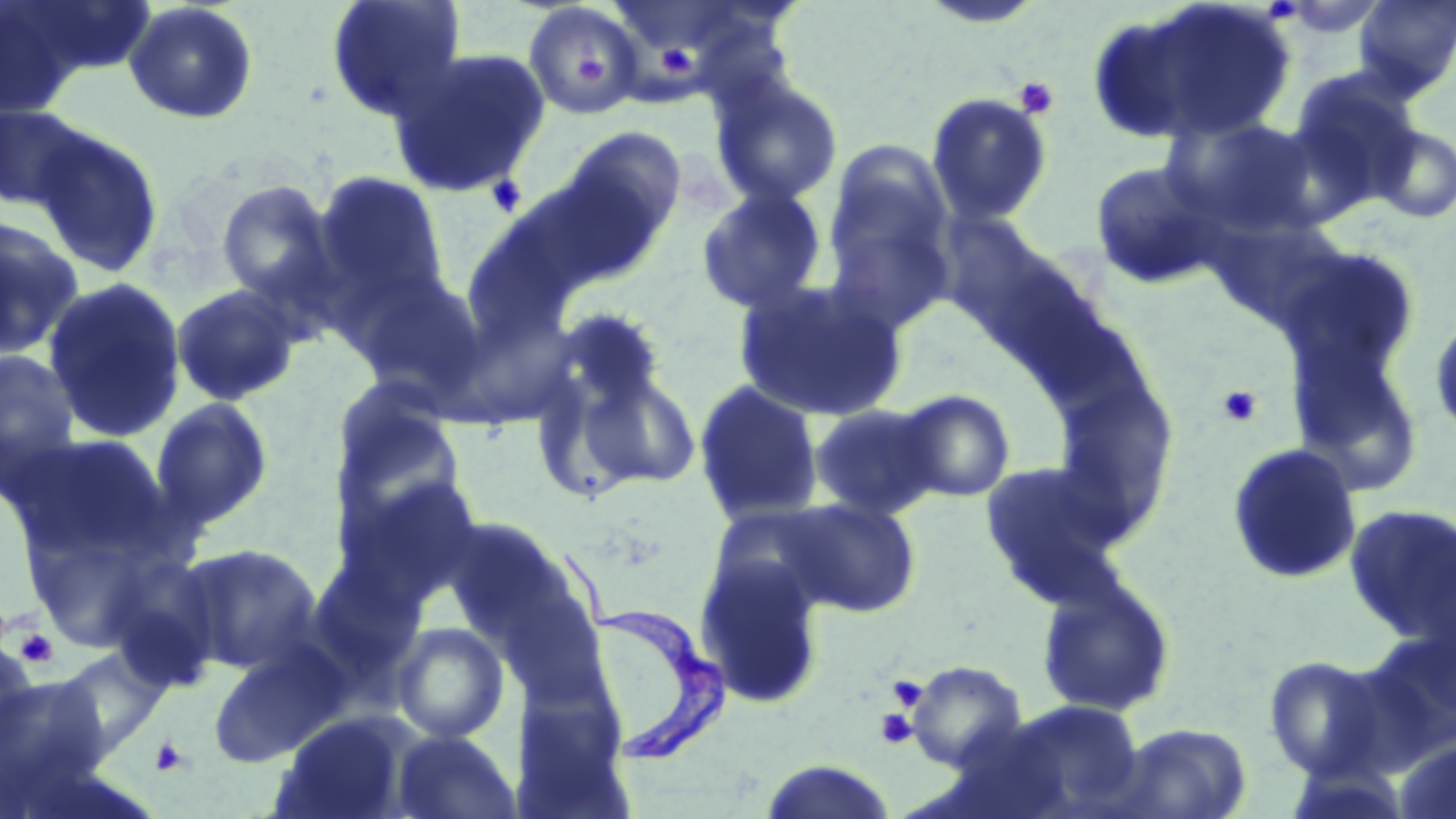
Approximate bounding boxes as [x1, y1, x2, y2] in pixels. Trypanosoma brucei locations: [585, 537, 729, 760]. Uninfected red blood cell locations: [2, 0, 155, 88], [324, 0, 468, 124], [1092, 0, 1298, 148], [1353, 0, 1456, 99], [122, 1, 260, 126], [1, 3, 88, 118], [522, 3, 644, 120], [388, 47, 551, 197], [1288, 69, 1423, 210], [709, 73, 844, 208], [925, 92, 1054, 226], [0, 102, 96, 213], [1163, 114, 1324, 239], [1371, 124, 1456, 224], [555, 126, 688, 262], [29, 127, 165, 278], [821, 144, 957, 329], [1090, 160, 1225, 289], [310, 170, 453, 322], [215, 178, 340, 310], [695, 186, 828, 315], [936, 213, 1085, 350], [0, 216, 85, 361], [1277, 245, 1422, 389], [346, 269, 491, 405], [42, 275, 187, 444], [733, 278, 909, 423], [170, 283, 303, 408], [552, 307, 671, 417], [1428, 312, 1456, 446], [1286, 338, 1425, 490], [0, 349, 83, 494], [556, 363, 703, 495], [1049, 372, 1181, 541], [692, 381, 825, 527], [330, 388, 466, 532], [892, 389, 1016, 504], [149, 397, 274, 533], [807, 403, 943, 520], [6, 433, 168, 561], [1225, 442, 1363, 585], [979, 458, 1136, 607], [334, 472, 486, 608], [778, 498, 922, 617], [1343, 503, 1456, 646], [440, 516, 582, 648], [175, 542, 323, 673], [695, 554, 826, 710], [1035, 574, 1177, 719], [499, 588, 609, 702], [391, 622, 510, 744], [207, 641, 350, 766], [0, 642, 42, 769], [55, 647, 170, 761], [1263, 654, 1390, 780], [907, 660, 1027, 771], [0, 670, 111, 800], [985, 698, 1146, 818], [276, 714, 412, 819], [1110, 722, 1253, 819], [390, 729, 521, 819], [1393, 736, 1456, 819], [756, 761, 899, 819]. Platelet locations: [655, 43, 697, 78], [578, 56, 612, 84], [1014, 76, 1060, 119], [486, 173, 528, 217], [1216, 385, 1263, 427], [13, 628, 59, 670], [887, 675, 927, 711], [875, 709, 918, 750], [149, 736, 191, 777]. Slide-level diagnosis: Trypanosoma brucei. Image is 1456×819 pixels. May-Grünwald-Giemsa-stained preparation. Thin blood smear. Captured at 1000x magnification. Light microscopy. Single field of view.